Outline each Plasmodium falciparum-infected red blood cell.
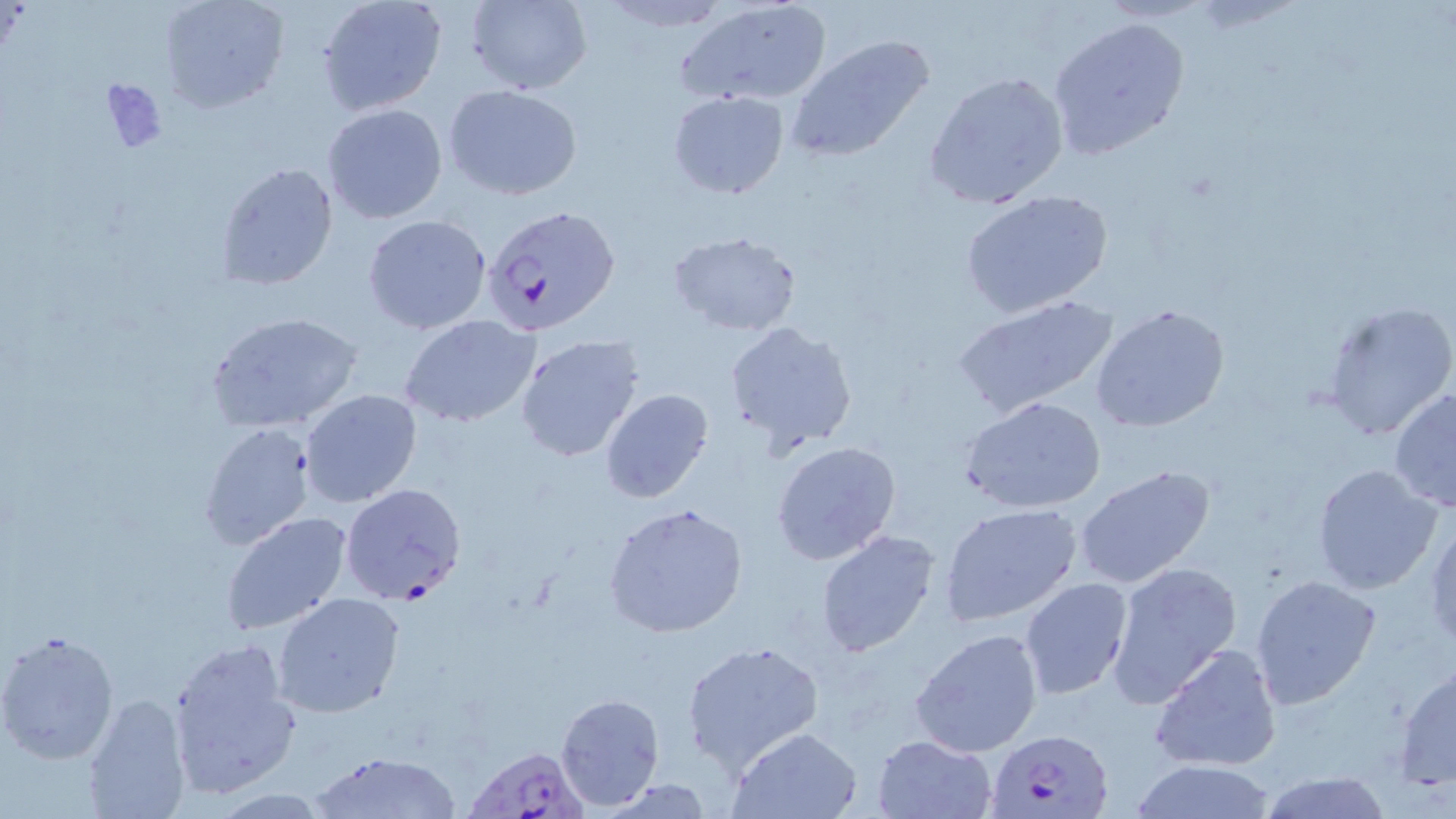
Approximate bounding boxes as [x1, y1, x2, y2] in pixels.
Plasmodium falciparum-infected red blood cells: [482, 205, 620, 338], [339, 482, 467, 605], [984, 728, 1115, 819], [462, 743, 587, 818].

slide-level diagnosis = Plasmodium falciparum
preparation = thin blood film
magnification = 1000x
modality = light microscopy
stain = May-Grünwald-Giemsa
image size = 1456×819 pixels
field of view = one of a larger specimen
uninfected red blood cell locations = approximate bounding boxes as [x1, y1, x2, y2] in pixels: [158, 0, 289, 115], [464, 0, 592, 93], [677, 0, 833, 107], [316, 1, 446, 116], [1048, 15, 1187, 159], [785, 35, 935, 163], [923, 68, 1070, 207], [444, 85, 583, 200], [668, 90, 788, 199], [322, 103, 449, 225], [215, 161, 340, 290], [961, 191, 1115, 320], [363, 213, 491, 335], [666, 230, 803, 336], [950, 294, 1119, 419], [1321, 301, 1456, 443], [1089, 304, 1231, 434], [205, 311, 364, 435], [399, 314, 540, 428], [721, 320, 857, 456], [515, 335, 645, 464], [1388, 386, 1456, 515], [599, 388, 715, 502], [298, 389, 422, 509], [962, 396, 1107, 515], [196, 422, 317, 550], [770, 440, 901, 566], [1075, 464, 1218, 591], [1309, 464, 1445, 596], [603, 501, 750, 637], [939, 503, 1081, 626], [220, 510, 352, 636], [1426, 516, 1456, 654], [814, 529, 941, 658], [1105, 561, 1242, 705], [1250, 573, 1383, 710], [1020, 578, 1135, 700], [272, 592, 407, 718], [0, 628, 121, 765], [909, 629, 1043, 759], [168, 638, 300, 799], [681, 639, 825, 772], [1149, 643, 1283, 773], [1393, 663, 1456, 789], [554, 691, 664, 809], [80, 693, 192, 819], [728, 726, 862, 818], [872, 733, 995, 818], [307, 750, 463, 819], [1128, 762, 1281, 819], [1255, 771, 1395, 819]